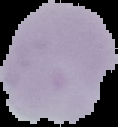

From a thin blood smear. Image is 118×127 pixels. Malaria status: uninfected. Cell region segmented out of the field of view; the surrounding area is masked to black.